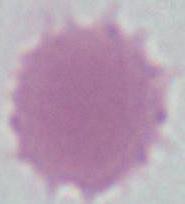

modality = photomicrograph
identification = red blood cell
magnification = 1000x